State which parasite is depicted.
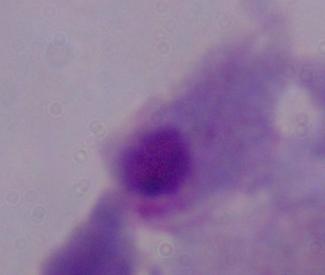

A trichomonad.

Captured at 1000x magnification. Photomicrograph.